Identify the blood parasite species.
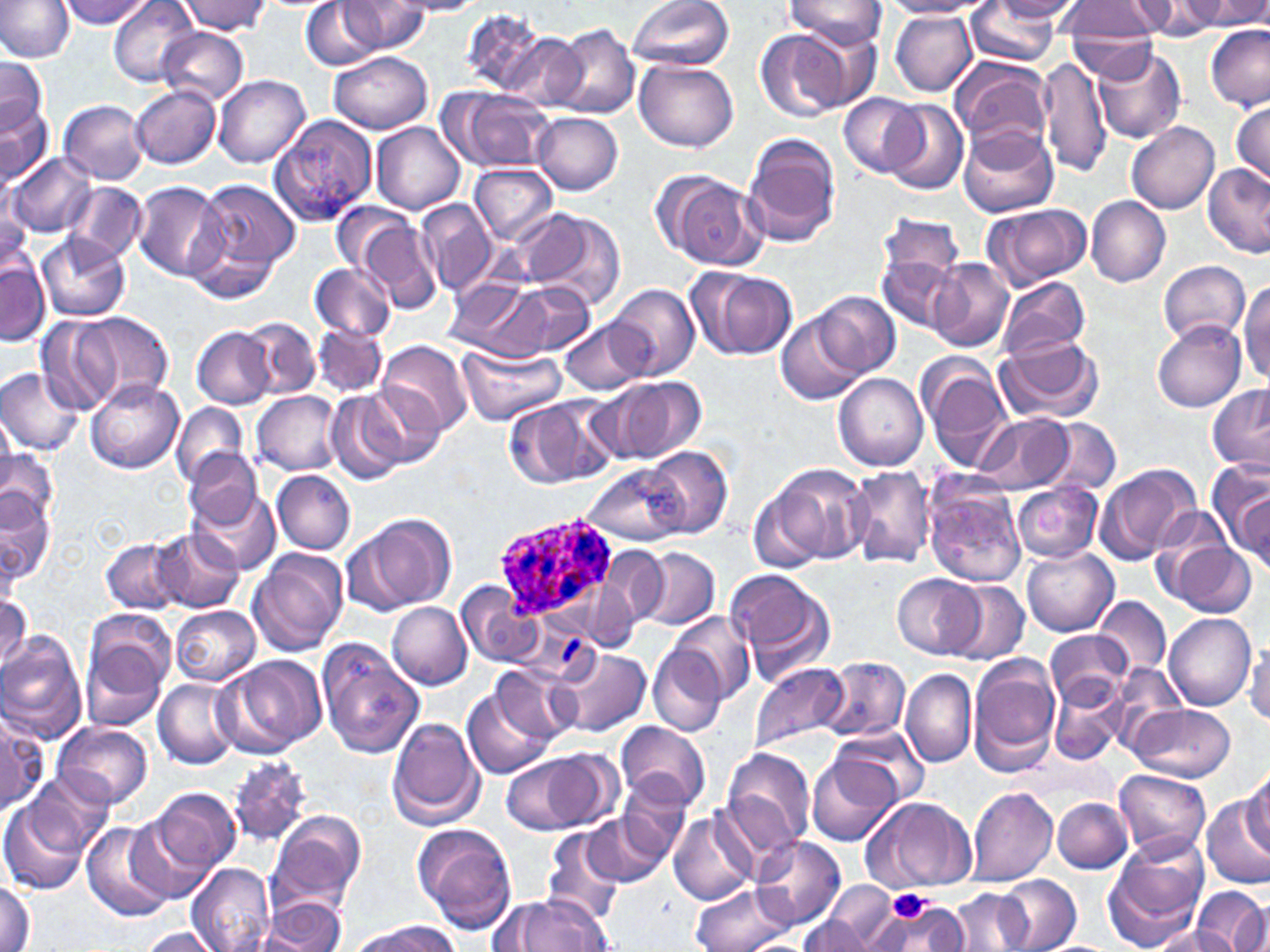

Plasmodium ovale.

stain = May-Grünwald-Giemsa
image size = 1270×952 pixels
Plasmodium ovale-infected red blood cell locations = approximate bounding boxes as (x1,y1)-(x2,y2) corner pairs in pixels: (495,515)-(623,624)
platelet locations = approximate bounding boxes as (x1,y1)-(x2,y2) corner pairs in pixels: (886,889)-(932,926)
magnification = 1000x
field of view = single
uninfected red blood cell locations = approximate bounding boxes as (x1,y1)-(x2,y2) corner pairs in pixels: (0,0)-(73,62), (63,0)-(150,29), (110,0)-(199,87), (390,0)-(483,16), (627,0)-(735,72), (784,0)-(887,52), (886,0)-(994,18), (992,0)-(1084,23), (1062,0)-(1163,50), (1130,0)-(1222,38), (1186,0)-(1270,30), (177,1)-(272,34), (302,1)-(382,70), (339,2)-(432,55), (964,3)-(1060,65), (461,8)-(547,93), (889,9)-(977,96), (791,23)-(880,113), (1067,23)-(1162,83), (552,24)-(639,119), (1203,25)-(1270,111), (156,27)-(249,105), (756,30)-(846,121), (496,31)-(588,111), (1095,44)-(1186,143), (328,51)-(433,133), (951,56)-(1055,156), (1040,56)-(1111,179), (0,59)-(46,138), (637,61)-(738,152), (214,75)-(310,168), (131,87)-(221,168), (440,87)-(555,173), (838,92)-(925,178), (1231,97)-(1270,188), (883,99)-(969,195), (0,100)-(52,188), (60,100)-(149,184), (533,112)-(623,195), (270,115)-(378,225), (1125,121)-(1219,215), (372,123)-(464,214), (957,126)-(1058,217), (741,134)-(840,248), (5,153)-(98,238), (470,163)-(558,244), (1202,163)-(1270,258), (655,169)-(767,271), (189,178)-(298,295), (64,181)-(147,264), (133,183)-(226,281), (1087,196)-(1171,286), (415,200)-(496,296), (333,201)-(415,279), (0,202)-(37,281), (982,202)-(1090,289), (877,211)-(962,301), (532,212)-(626,313), (350,216)-(440,314), (36,233)-(130,322), (877,248)-(963,332), (1,258)-(49,347), (930,260)-(1013,353), (1159,260)-(1250,345), (310,262)-(396,341), (690,266)-(796,359), (996,275)-(1091,361), (461,278)-(588,361), (1238,281)-(1270,385), (608,283)-(699,379), (813,291)-(900,378), (50,310)-(177,413), (777,315)-(862,406), (242,317)-(321,399), (559,319)-(652,395), (1153,322)-(1245,411), (314,323)-(385,395), (193,326)-(274,409), (995,335)-(1104,424), (379,341)-(472,439), (457,346)-(566,425), (919,358)-(1013,468), (1,367)-(85,455), (834,373)-(927,469), (86,377)-(182,473), (617,379)-(705,462), (362,382)-(446,469), (1206,384)-(1270,473), (252,390)-(341,476), (325,390)-(406,484), (504,398)-(610,490), (172,403)-(248,488), (0,412)-(17,496), (974,414)-(1071,494), (1042,418)-(1120,496), (645,444)-(732,538), (2,446)-(57,536), (184,449)-(265,532), (1094,463)-(1199,566), (586,465)-(683,546), (770,465)-(871,567), (847,467)-(936,567), (272,469)-(356,555), (925,482)-(1027,587), (1012,482)-(1103,564), (750,484)-(831,575), (1229,484)-(1269,570), (192,485)-(279,574), (1,488)-(53,588), (1149,508)-(1240,605), (354,514)-(455,614), (152,529)-(243,614), (102,538)-(183,614), (1168,540)-(1256,619), (602,546)-(670,626), (1022,546)-(1119,639), (639,547)-(719,630), (249,548)-(349,659), (729,569)-(834,682), (893,573)-(983,658), (947,580)-(1029,664), (457,581)-(540,667), (584,581)-(640,652), (0,592)-(31,674), (1094,597)-(1171,677), (386,602)-(471,690), (171,605)-(261,687), (164,608)-(252,766), (666,611)-(754,704), (1165,613)-(1255,711), (1043,629)-(1131,708), (80,631)-(171,730), (0,632)-(87,743), (317,641)-(423,759), (1246,642)-(1270,727), (648,647)-(729,737), (554,650)-(650,737), (969,653)-(1062,771), (222,656)-(328,757), (822,657)-(910,743), (750,662)-(849,754), (490,664)-(581,746), (900,670)-(975,768), (153,678)-(240,768), (1053,681)-(1129,765), (462,686)-(553,780), (1127,704)-(1235,783), (1,712)-(48,815), (388,718)-(484,831), (53,721)-(152,811), (617,721)-(709,809), (836,727)-(926,808), (722,749)-(817,854), (503,753)-(601,835), (809,755)-(899,847), (225,758)-(312,846), (1244,767)-(1270,858), (1114,768)-(1211,861), (26,771)-(113,858), (618,773)-(697,858), (146,787)-(240,879), (966,787)-(1058,886), (871,797)-(978,893), (1053,798)-(1132,872), (1203,798)-(1270,890), (0,799)-(92,895), (670,809)-(755,906), (123,811)-(219,905), (266,812)-(368,918), (583,813)-(666,885), (82,822)-(173,921), (413,823)-(517,933), (542,826)-(625,925), (1108,834)-(1210,945), (752,835)-(846,928), (188,862)-(275,952), (996,874)-(1080,950), (0,879)-(34,952), (691,883)-(793,952), (819,883)-(901,948), (950,887)-(1033,952), (1192,887)-(1270,952), (862,893)-(961,952), (505,895)-(613,951), (263,897)-(346,951), (487,897)-(555,949), (1230,899)-(1269,952), (798,912)-(874,951), (354,921)-(457,952), (1151,925)-(1237,952), (137,927)-(221,951)
modality = light microscopy
preparation = thin blood smear